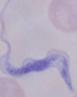
A trypanosome is shown. Photomicrograph. 1000x magnification.